Assess the morphology of the erythrocytes.
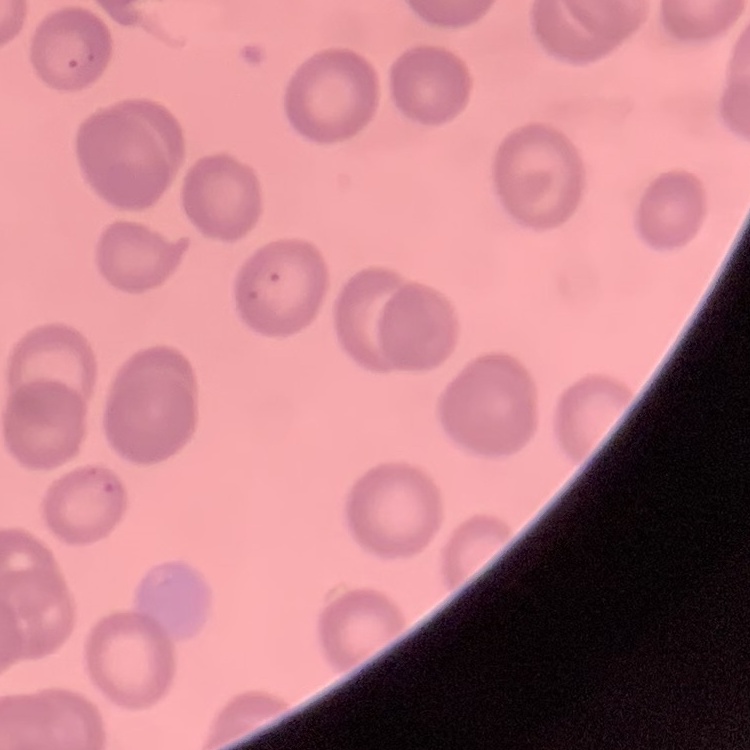
They show no rouleaux formation.

Stained with either Field's or Giemsa. Square crop of a larger photomicrograph. Thin blood smear.